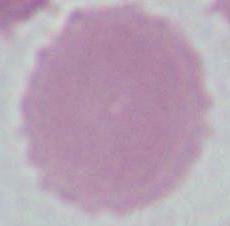
identification = red blood cell
magnification = 1000x
modality = photomicrograph